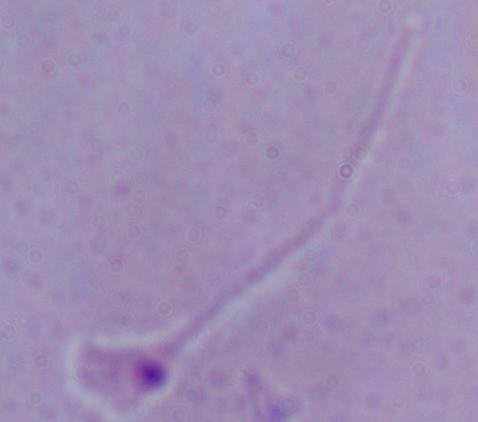

1000x magnification. A Leishmania parasite is seen. Micrograph.